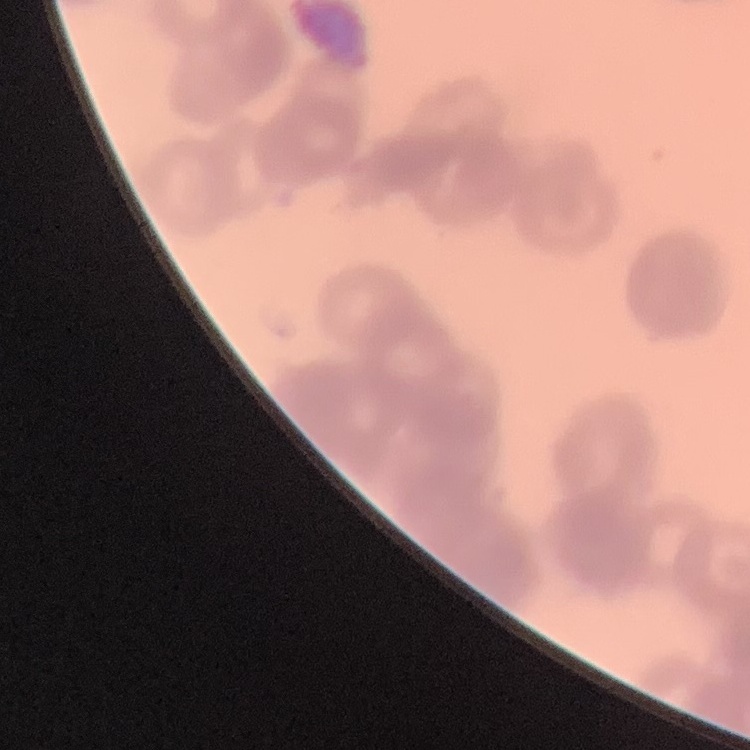

erythrocyte morphology = rouleaux formation
preparation = thin peripheral smear
image type = one tile cut from a larger photomicrograph
stain = Field's or Giemsa